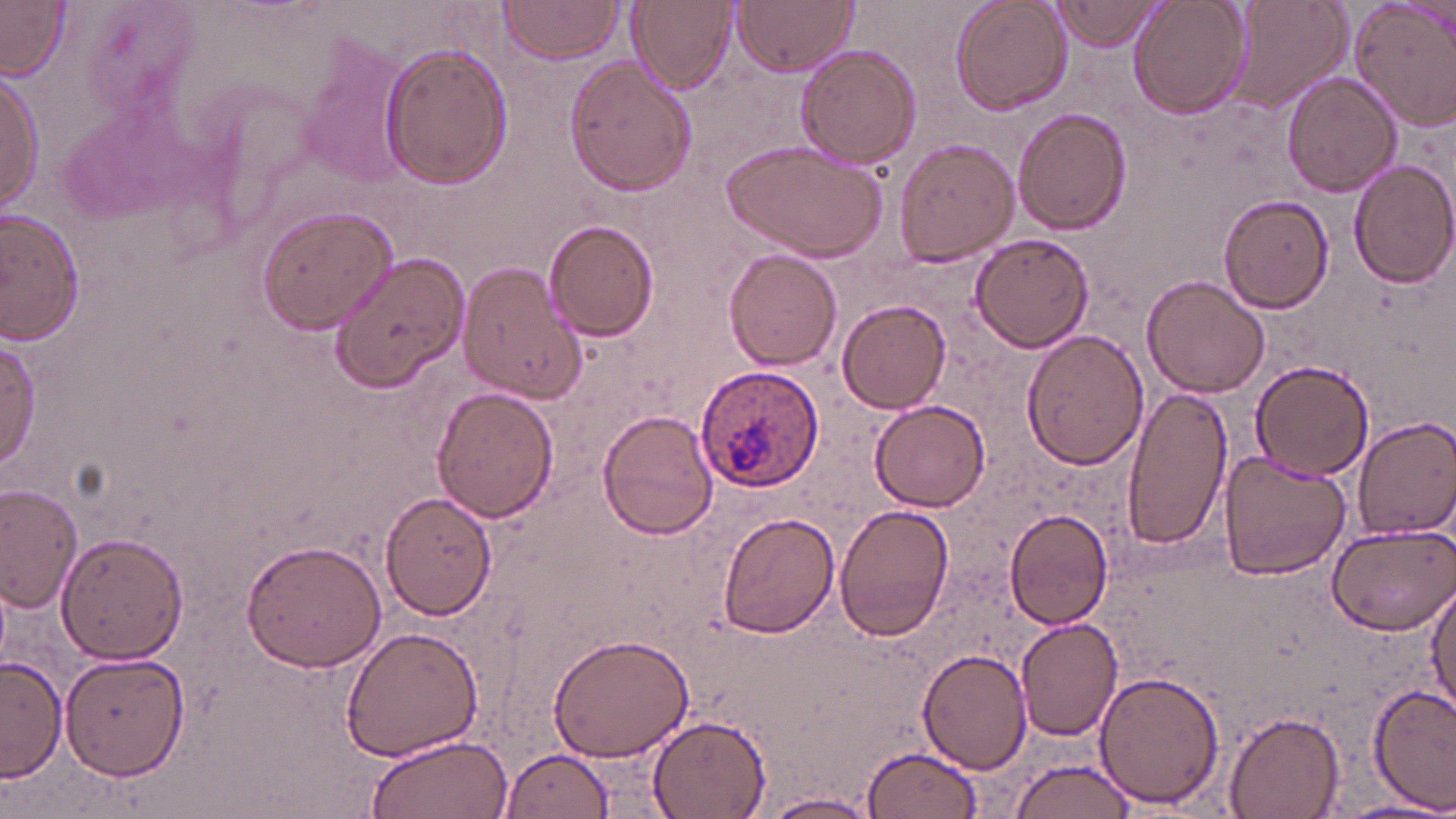
{
  "slide_level_diagnosis": "Plasmodium ovale",
  "preparation": "thin blood film",
  "plasmodium_ovale_infected_red_blood_cell_locations": "approximate bounding boxes as (x1,y1)-(x2,y2) corner pairs in pixels: (694,362)-(824,496)",
  "magnification": "1000x",
  "stain": "May-Grünwald-Giemsa",
  "modality": "light microscopy",
  "field_of_view": "one of a larger specimen",
  "uninfected_red_blood_cell_locations": "approximate bounding boxes as (x1,y1)-(x2,y2) corner pairs in pixels: (631,0)-(737,93), (732,0)-(858,78), (951,0)-(1071,115), (1128,0)-(1253,119), (1229,0)-(1349,113), (1350,0)-(1456,132), (0,1)-(72,79), (497,1)-(621,64), (1047,1)-(1165,51), (294,34)-(414,190), (379,38)-(511,189), (795,44)-(921,168), (564,56)-(695,196), (1,69)-(45,215), (1283,72)-(1401,195), (1013,108)-(1131,234), (893,136)-(1019,267), (721,141)-(886,264), (1349,160)-(1456,285), (1218,194)-(1335,312), (2,206)-(88,346), (255,206)-(398,335), (543,220)-(659,342), (971,231)-(1094,353), (725,249)-(843,369), (329,251)-(470,395), (455,257)-(588,404), (1142,274)-(1272,396), (837,300)-(952,413), (1021,328)-(1147,469), (0,337)-(40,471), (1250,361)-(1376,482), (1119,384)-(1231,552), (433,386)-(560,521), (872,399)-(992,511), (597,409)-(721,540), (1353,415)-(1456,537), (1217,451)-(1353,580), (0,484)-(82,612), (380,492)-(496,620), (834,504)-(954,643), (1003,508)-(1115,629), (716,512)-(838,638), (1324,523)-(1456,634), (55,532)-(188,664), (239,537)-(388,671), (1427,578)-(1456,718), (1015,615)-(1123,739), (339,623)-(483,763), (547,634)-(694,762), (917,647)-(1033,774), (60,649)-(188,780), (2,657)-(65,781), (1093,669)-(1224,810), (1369,685)-(1456,813), (1221,709)-(1345,817), (644,715)-(770,818), (363,735)-(513,819), (857,744)-(985,818), (499,747)-(615,817), (1005,752)-(1141,819), (765,792)-(880,817), (1333,798)-(1456,819)",
  "image_size": "1456×819 pixels"
}